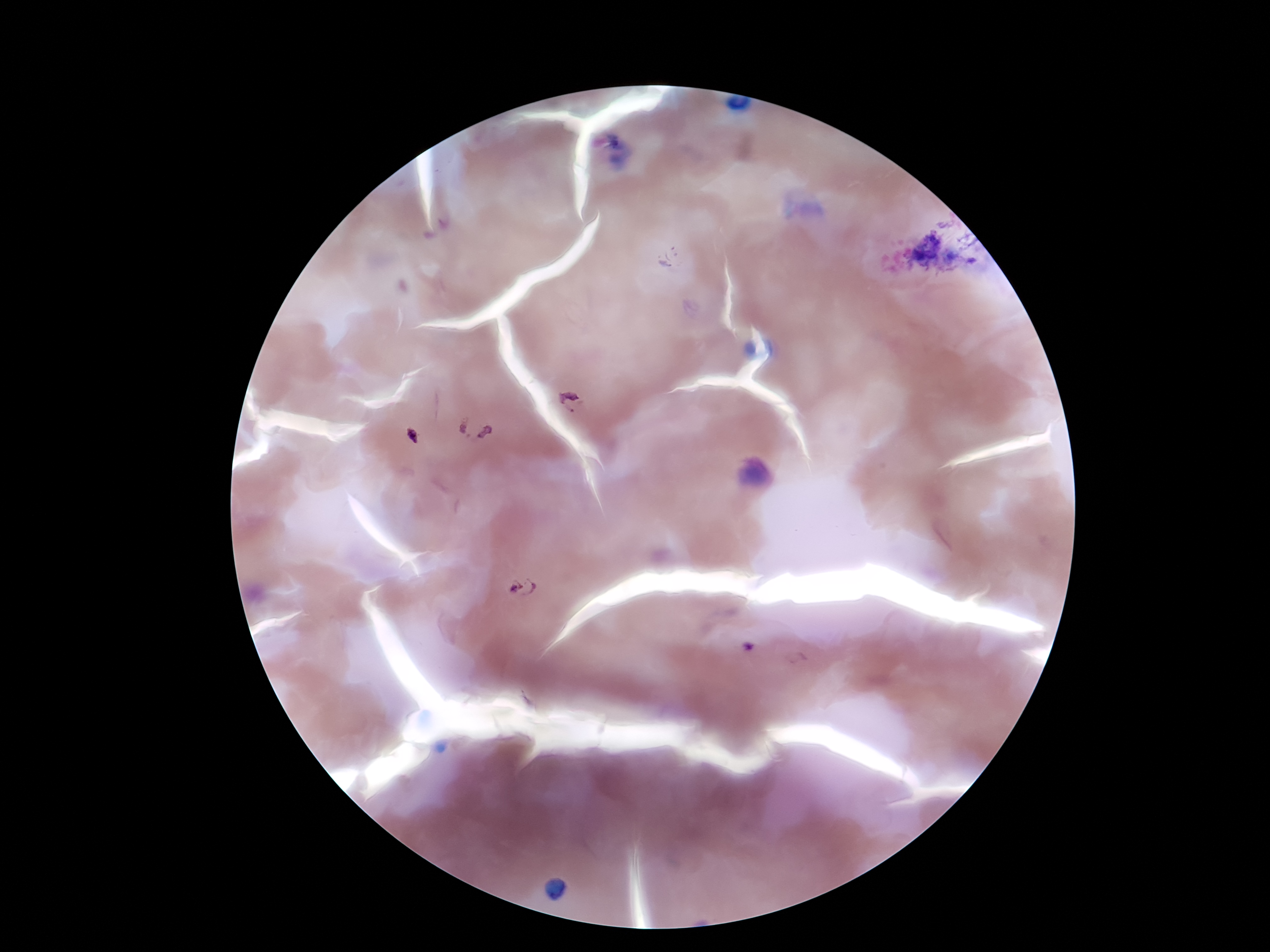
Approximate centers as [x, y] in pixels. Plasmodium parasite locations: [574, 400], [475, 428], [522, 587]. Image is 1270×952 pixels. Thick peripheral-blood smear. 100x magnification. Single field of view. Smartphone photograph taken through the microscope eyepiece. Giemsa stain. Patient malaria status: positive.